Assess this cell for malaria.
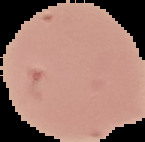

It is uninfected.

Image is 145×142 pixels. Segmented cell region on a black background. From a thin blood smear.